Report the malaria status of this cell.
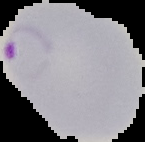

It is parasitized.

Summary:
  - Image type: segmented cell region with the area outside set to black
  - Image size: 145×142 pixels
  - Preparation: thin blood smear